State which parasite is depicted.
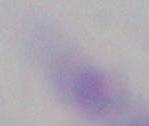

Toxoplasma gondii.

Micrograph. Captured at 1000x magnification.